Locate every blood parasite and identify its species.
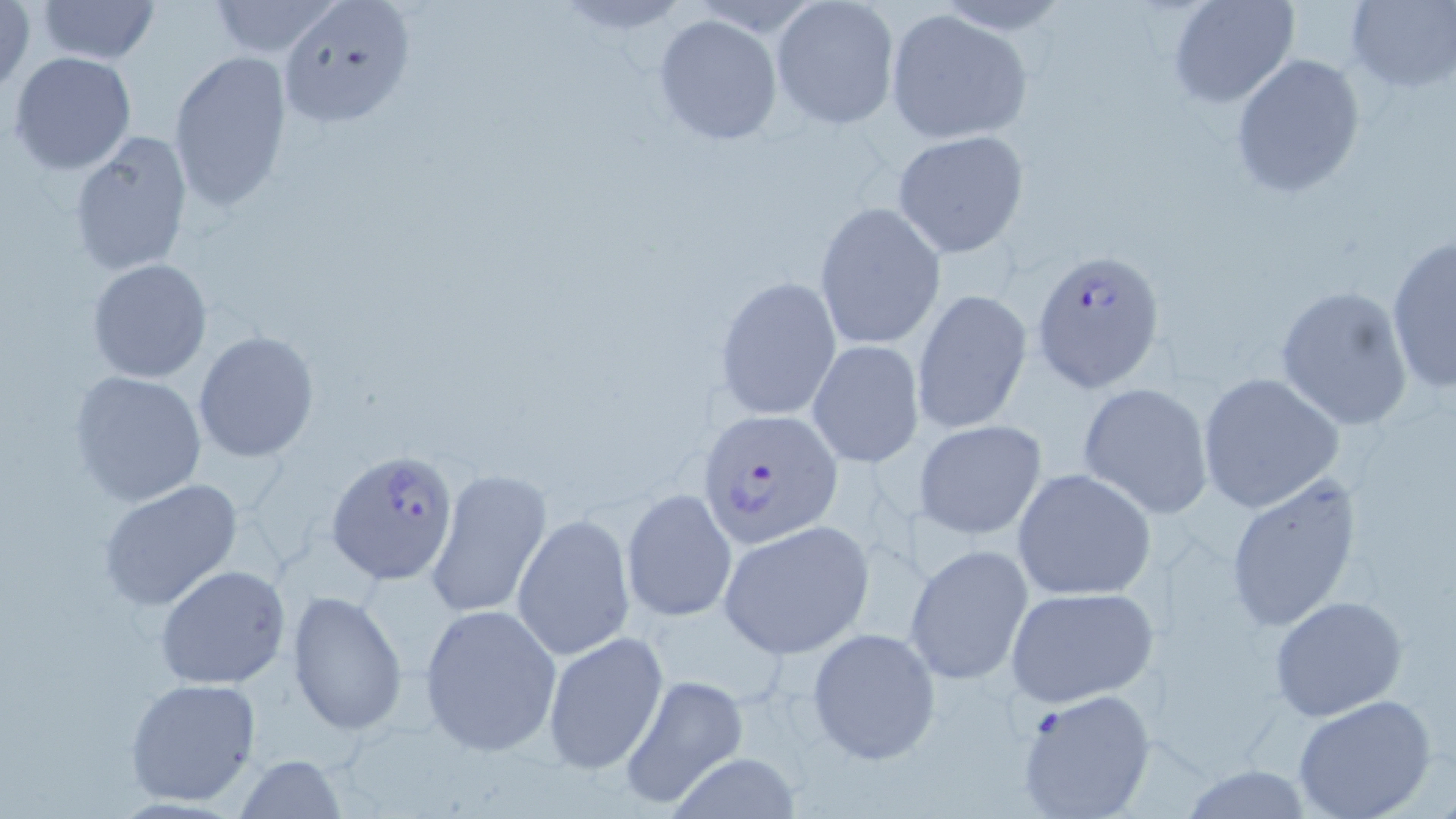

Approximate bounding boxes as [x1, y1, x2, y2] in pixels.
Plasmodium falciparum-infected red blood cells: [1032, 247, 1167, 395], [697, 408, 844, 550], [325, 448, 460, 583].
No Plasmodium ovale, Plasmodium malariae, Plasmodium vivax, Babesia divergens, or Trypanosoma brucei observed.

slide-level diagnosis = Plasmodium falciparum
modality = light microscopy
preparation = thin blood film
field of view = single
stain = May-Grünwald-Giemsa
uninfected red blood cell locations = approximate bounding boxes as [x1, y1, x2, y2] in pixels: [38, 0, 158, 66], [205, 0, 344, 58], [1166, 0, 1300, 108], [1344, 0, 1456, 90], [1, 1, 36, 94], [770, 1, 901, 131], [279, 3, 414, 129], [884, 10, 1033, 144], [652, 13, 784, 146], [7, 51, 137, 175], [169, 51, 293, 212], [1231, 53, 1365, 199], [892, 129, 1030, 257], [67, 130, 192, 275], [814, 201, 946, 351], [1386, 231, 1455, 393], [86, 257, 214, 383], [714, 275, 842, 420], [1273, 284, 1415, 432], [913, 289, 1033, 437], [193, 330, 321, 465], [807, 341, 924, 467], [68, 371, 206, 507], [1196, 372, 1344, 514], [1078, 381, 1213, 518], [915, 418, 1048, 540], [424, 466, 550, 623], [1011, 467, 1156, 602], [1226, 472, 1368, 631], [97, 479, 244, 612], [622, 488, 738, 623], [513, 513, 634, 659], [719, 521, 873, 657], [906, 543, 1032, 685], [154, 563, 292, 689], [1003, 585, 1158, 708], [286, 589, 408, 735], [1267, 595, 1407, 720], [418, 602, 561, 757], [807, 627, 940, 765], [543, 630, 670, 774], [619, 674, 749, 808], [124, 676, 262, 806], [1014, 688, 1155, 818], [1292, 694, 1438, 819], [233, 754, 349, 818], [663, 754, 807, 819]
image size = 1456×819 pixels
magnification = 1000x